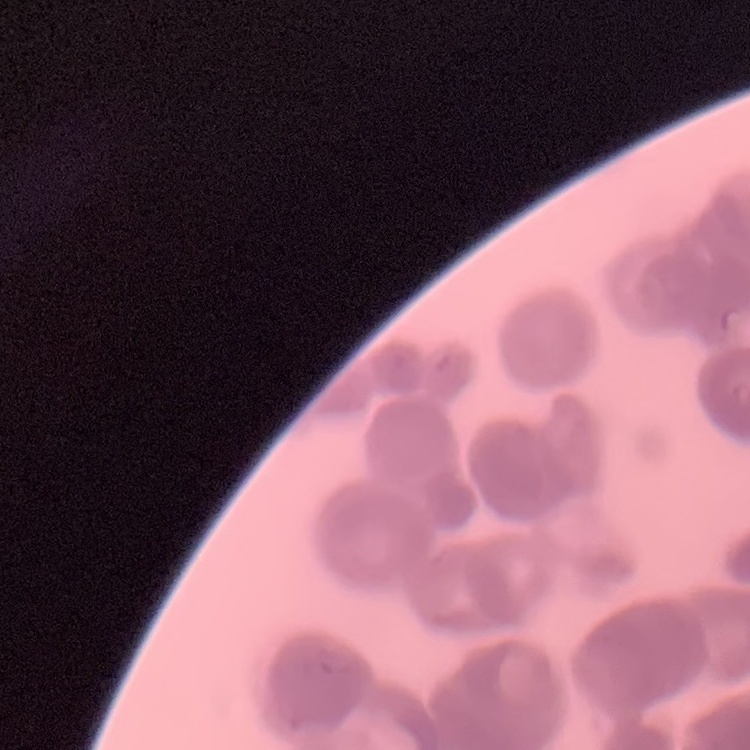

The red blood cells show rouleaux formation. Square crop of a larger photomicrograph. Thin peripheral smear. Field's or Giemsa stain.